Assess this cell for malaria.
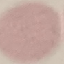
Uninfected.

stain = Giemsa
image type = automatically extracted cell patch, resized to 64 × 64 pixels
preparation = thin blood film
capture = smartphone through the microscope eyepiece